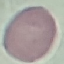

result = no malaria parasites detected
capture = smartphone through the microscope eyepiece
preparation = thin blood smear
stain = Giemsa
image type = cell patch, automatically extracted from a larger field of view and resized to 64 × 64 pixels